Describe the morphology of the erythrocytes.
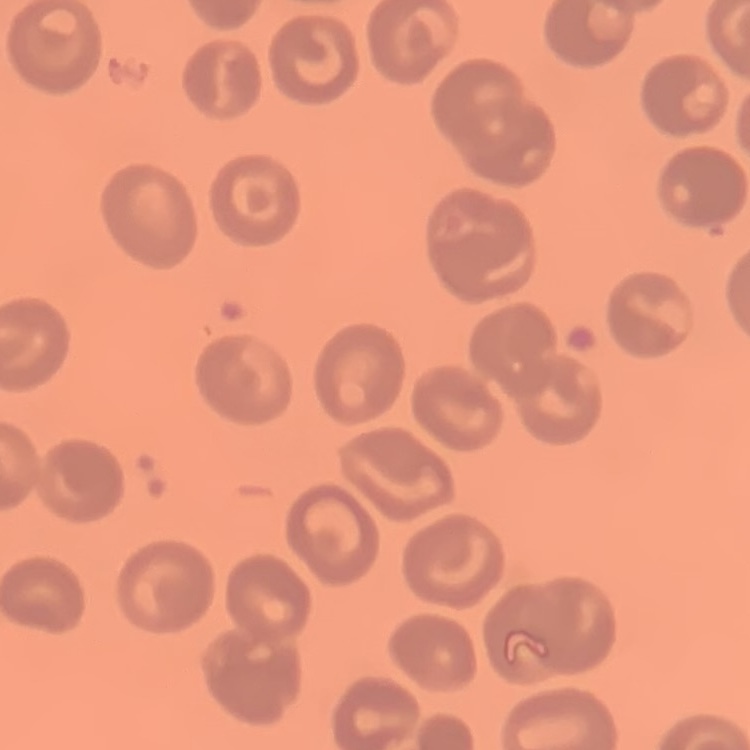

No rouleaux formation.

{
  "preparation": "thin blood film",
  "stain": "Field's or Giemsa",
  "image_type": "square crop of a larger photomicrograph"
}